Outline each blood parasite and name the species.
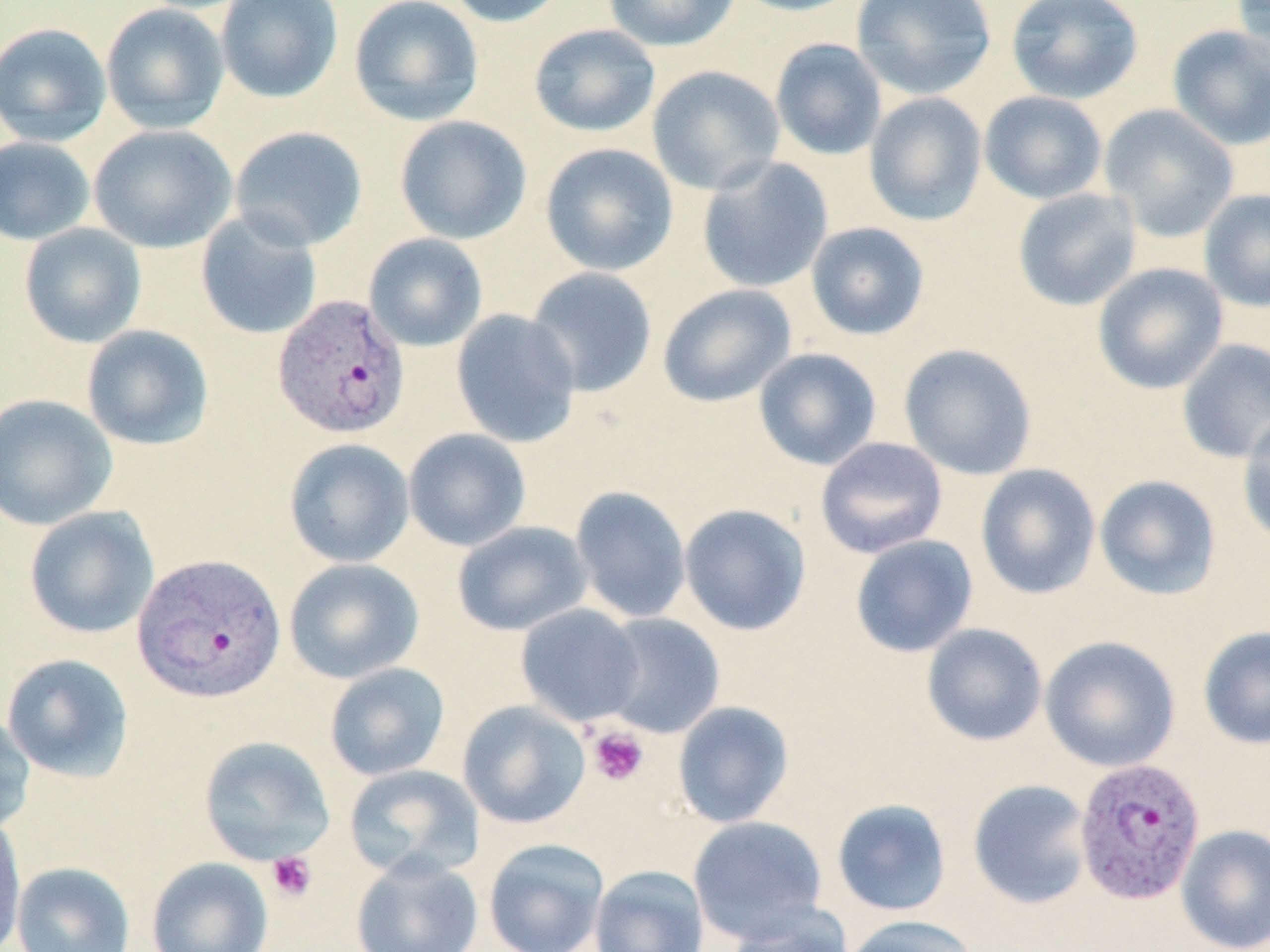

Approximate bounding boxes as named x1/y1/x2/y2 corners in pixels.
Plasmodium vivax-infected red blood cells: (x1=272, y1=293, x2=410, y2=439), (x1=133, y1=552, x2=286, y2=704), (x1=1073, y1=757, x2=1206, y2=906).
No Plasmodium falciparum, Plasmodium ovale, Plasmodium malariae, Babesia divergens, or Trypanosoma brucei observed.

Platelet locations: (x1=587, y1=725, x2=649, y2=787), (x1=266, y1=851, x2=318, y2=902). Uninfected red blood cell locations: (x1=215, y1=0, x2=344, y2=104), (x1=349, y1=0, x2=484, y2=127), (x1=444, y1=0, x2=569, y2=27), (x1=602, y1=0, x2=741, y2=52), (x1=728, y1=0, x2=865, y2=17), (x1=851, y1=0, x2=997, y2=100), (x1=1006, y1=0, x2=1144, y2=104), (x1=1231, y1=0, x2=1270, y2=63), (x1=100, y1=2, x2=229, y2=134), (x1=0, y1=22, x2=112, y2=147), (x1=528, y1=24, x2=660, y2=138), (x1=1166, y1=25, x2=1270, y2=151), (x1=770, y1=38, x2=887, y2=160), (x1=647, y1=65, x2=786, y2=195), (x1=979, y1=91, x2=1107, y2=205), (x1=864, y1=92, x2=987, y2=226), (x1=1099, y1=104, x2=1240, y2=242), (x1=394, y1=115, x2=532, y2=244), (x1=88, y1=124, x2=237, y2=254), (x1=229, y1=126, x2=368, y2=252), (x1=0, y1=137, x2=95, y2=245), (x1=540, y1=143, x2=678, y2=276), (x1=697, y1=156, x2=833, y2=293), (x1=1012, y1=187, x2=1142, y2=312), (x1=1199, y1=188, x2=1270, y2=313), (x1=195, y1=211, x2=323, y2=340), (x1=806, y1=222, x2=930, y2=341), (x1=19, y1=223, x2=147, y2=348), (x1=363, y1=232, x2=488, y2=352), (x1=1092, y1=262, x2=1229, y2=395), (x1=525, y1=267, x2=658, y2=398), (x1=657, y1=284, x2=796, y2=407), (x1=451, y1=309, x2=582, y2=448), (x1=81, y1=324, x2=215, y2=450), (x1=1176, y1=338, x2=1270, y2=464), (x1=899, y1=343, x2=1038, y2=480), (x1=753, y1=348, x2=882, y2=470), (x1=0, y1=393, x2=118, y2=530), (x1=1237, y1=413, x2=1270, y2=545), (x1=403, y1=428, x2=531, y2=551), (x1=815, y1=436, x2=948, y2=559), (x1=284, y1=438, x2=415, y2=568), (x1=975, y1=463, x2=1101, y2=600), (x1=1094, y1=474, x2=1222, y2=600), (x1=569, y1=485, x2=692, y2=623), (x1=679, y1=503, x2=812, y2=636), (x1=24, y1=506, x2=160, y2=639), (x1=452, y1=520, x2=592, y2=636), (x1=850, y1=534, x2=978, y2=658), (x1=283, y1=558, x2=424, y2=684), (x1=515, y1=604, x2=646, y2=727), (x1=598, y1=612, x2=725, y2=739), (x1=921, y1=623, x2=1048, y2=746), (x1=1198, y1=625, x2=1270, y2=749), (x1=1040, y1=635, x2=1181, y2=772), (x1=1, y1=653, x2=135, y2=782), (x1=324, y1=662, x2=450, y2=781), (x1=457, y1=700, x2=591, y2=829), (x1=672, y1=701, x2=794, y2=828), (x1=0, y1=711, x2=36, y2=835), (x1=198, y1=735, x2=335, y2=865), (x1=343, y1=764, x2=484, y2=880), (x1=967, y1=779, x2=1094, y2=910), (x1=831, y1=798, x2=952, y2=917), (x1=0, y1=813, x2=26, y2=952), (x1=688, y1=815, x2=829, y2=943), (x1=1176, y1=824, x2=1270, y2=952), (x1=482, y1=838, x2=609, y2=952), (x1=350, y1=853, x2=484, y2=952), (x1=146, y1=857, x2=274, y2=952), (x1=11, y1=860, x2=136, y2=952), (x1=590, y1=864, x2=710, y2=952), (x1=723, y1=902, x2=854, y2=952), (x1=843, y1=915, x2=981, y2=952). Slide-level diagnosis: Plasmodium vivax. Optical microscopy. One field of a larger specimen. Captured at 1000x magnification. Thin blood smear. Image is 1270×952 pixels. May-Grünwald-Giemsa stain.